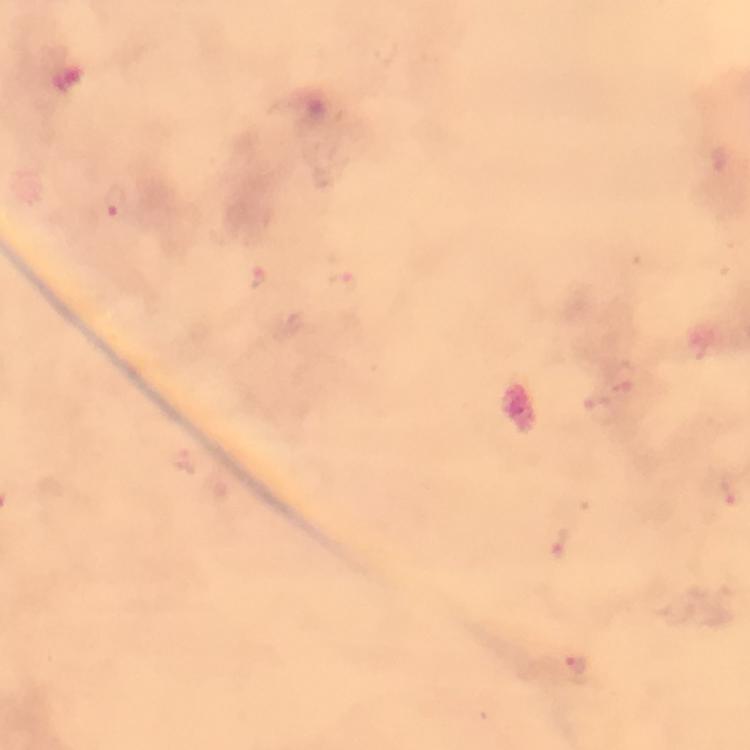
image size = 750×750 pixels
malaria parasite locations = approximate object centers, in pixels from the top-left corner: (x=718, y=160), (x=114, y=203), (x=259, y=277), (x=343, y=283), (x=596, y=403), (x=729, y=492), (x=560, y=542), (x=574, y=664)
context = from a malaria diagnostic workup
preparation = thick blood smear
stain = Giemsa
capture = smartphone mounted on the microscope
immersion oil = used
magnification = 100x
cropped from = one field of view